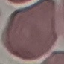
Malaria status: uninfected. Giemsa-stained preparation. Acquired by smartphone through the microscope eyepiece. Cell patch, automatically extracted from a larger field of view and resized to 64 × 64 pixels. Thin smear of blood.